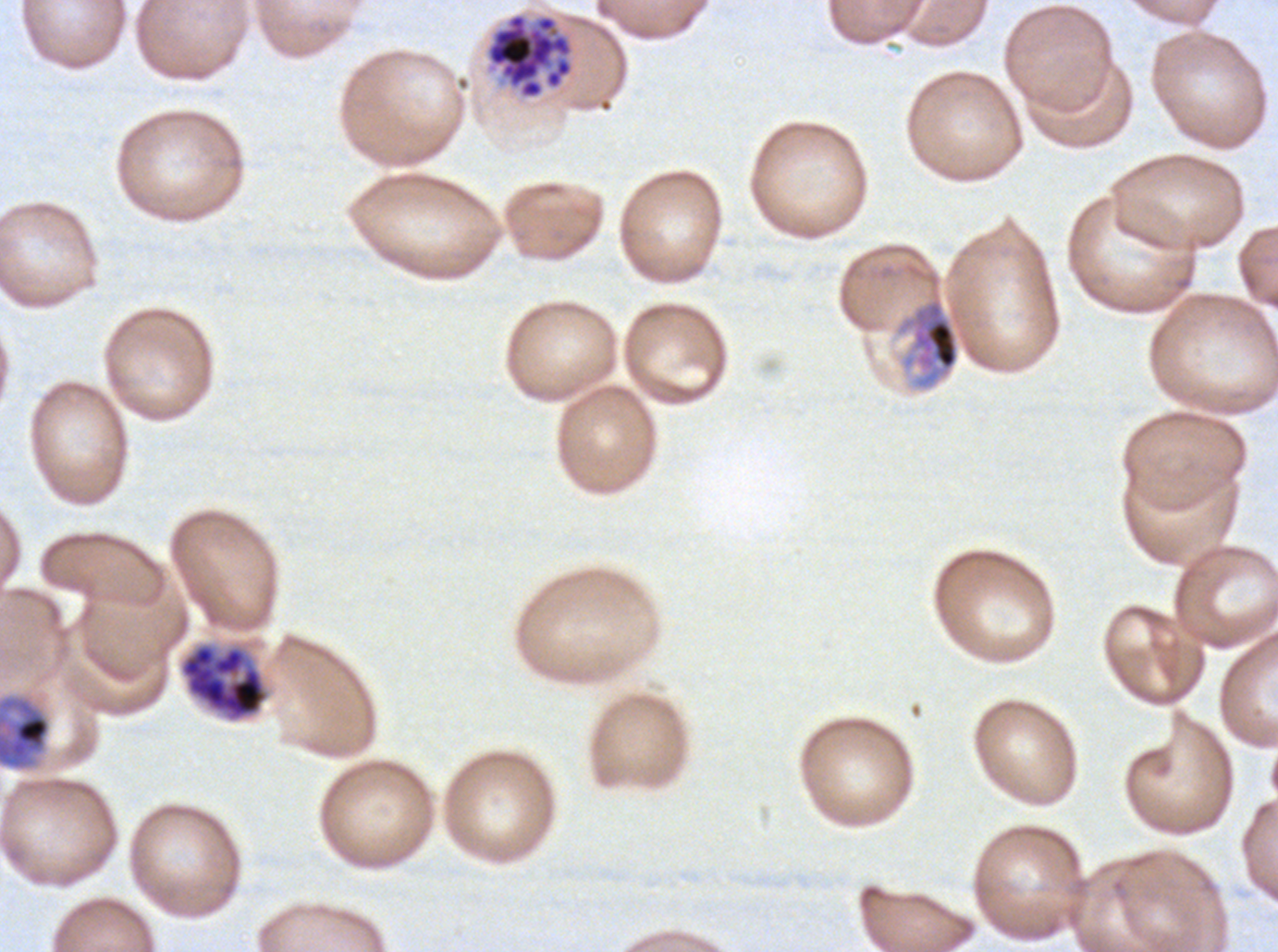
Approximate bounding boxes as {x1, y1, x2, y2} in pixels. Segmenter locations: {485, 11, 575, 100}. Late schizont locations: {179, 643, 269, 721}. Late trophozoite locations: {897, 296, 960, 389}, {0, 696, 51, 770}. Giemsa stain. Image is 1278×952 pixels. Thin blood film. Life-cycle stages observed: late trophozoite, late schizont, segmenter. Ex-vivo P. falciparum culture from a patient in The Gambia, grown for 24 to 48 hours. A sub-image separated from a larger composite.